Report the malaria status of this cell.
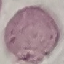

It is uninfected.

{
  "preparation": "thin smear",
  "stain": "Giemsa",
  "image_type": "cell patch, automatically extracted from a larger field of view and resized to 64 × 64 pixels",
  "capture": "smartphone through the microscope eyepiece"
}